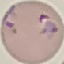

Summary:
  - Result: malaria parasites identified
  - Preparation: thin blood film
  - Stain: Giemsa
  - Capture: smartphone camera at the microscope eyepiece
  - Image type: automatically extracted cell patch, resized to 64 × 64 pixels